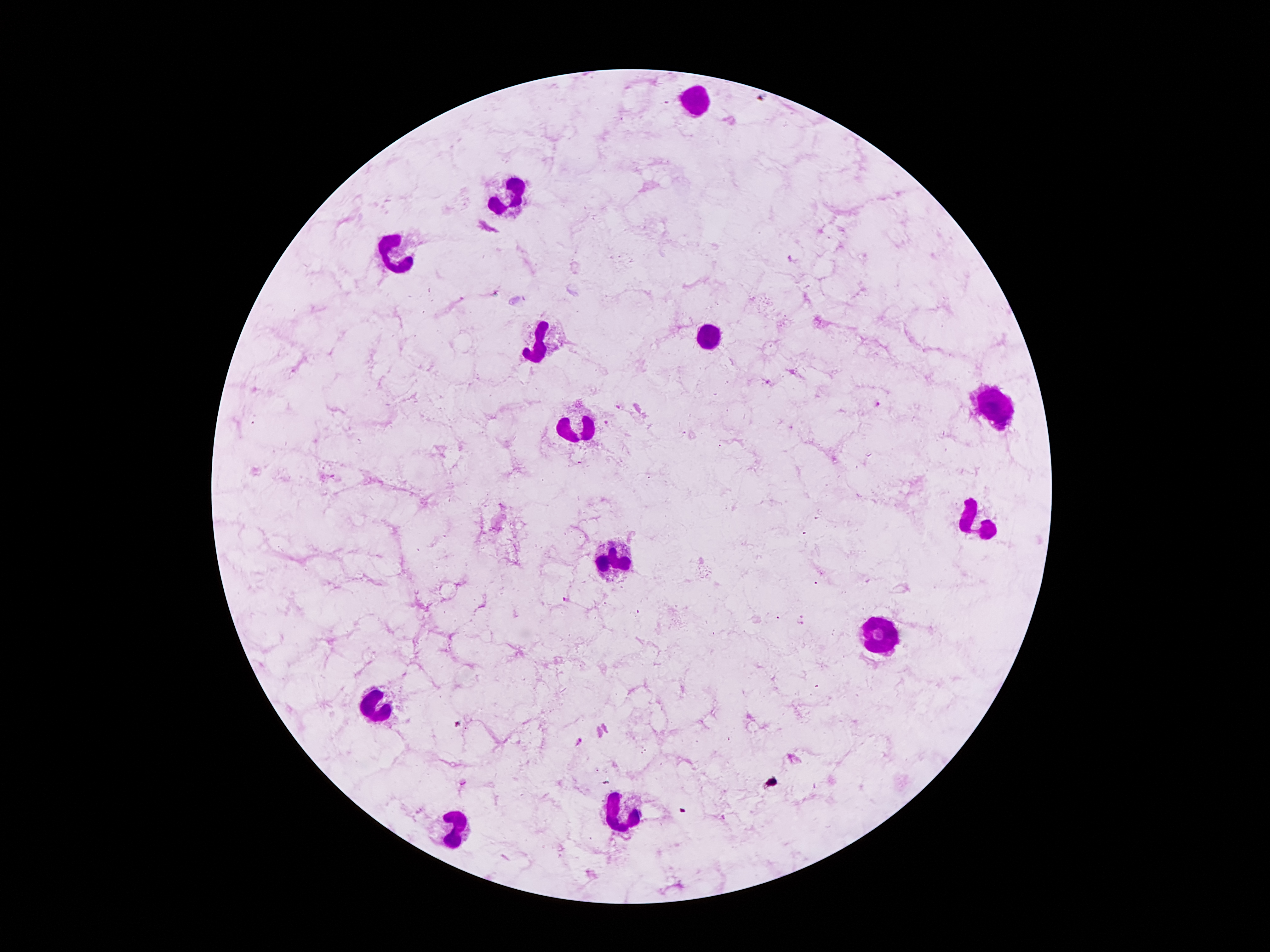

{
  "leukocyte_locations": "approximate centers as (x, y) in pixels: (696, 99), (511, 195), (400, 256), (708, 338), (542, 345), (994, 408), (576, 431), (981, 523), (618, 555), (880, 636), (381, 702), (626, 811), (456, 832)",
  "magnification": "100x",
  "field_of_view": "one from this slide",
  "capture": "smartphone camera through the microscope eyepiece",
  "image_size": "1270×952 pixels",
  "preparation": "thick blood smear",
  "patient_malaria_status": "positive for Plasmodium falciparum",
  "stain": "Giemsa",
  "plasmodium_parasite_locations": "approximate centers as (x, y) in pixels: (767, 382), (878, 405), (618, 407), (606, 422), (567, 599), (803, 615), (799, 624), (459, 725), (578, 740)"
}